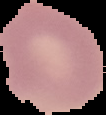
image size = 106×115 pixels
preparation = thin blood film
image type = segmented cell region with the area outside set to black
malaria status = uninfected